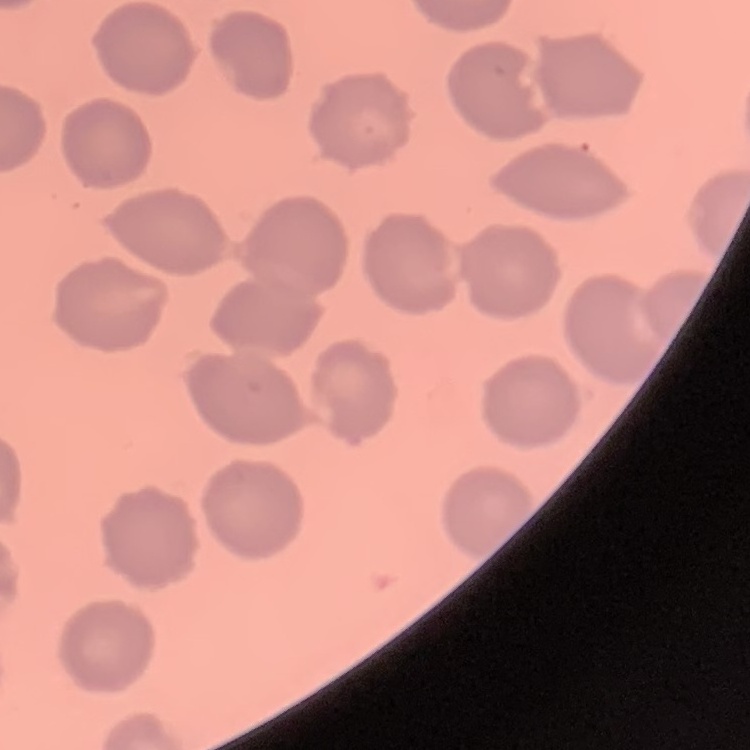
The red blood cells show no rouleaux formation. Stained with either Field's or Giemsa. Square crop of a larger photomicrograph. Thin blood film.